Assess the morphology of the red blood cells.
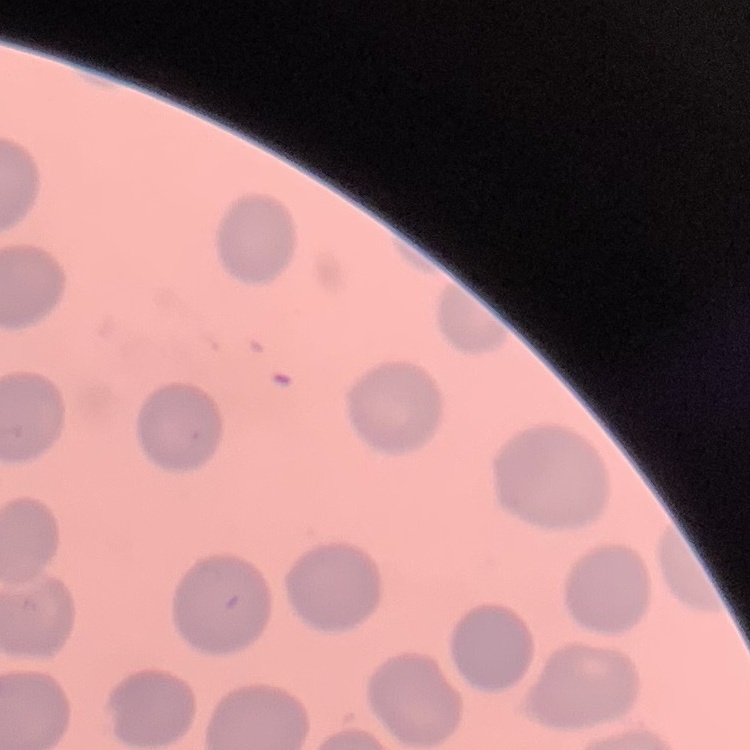
They show no rouleaux formation.

preparation = thin blood film
stain = Field's or Giemsa
image type = one tile cut from a larger photomicrograph